Identify the parasite.
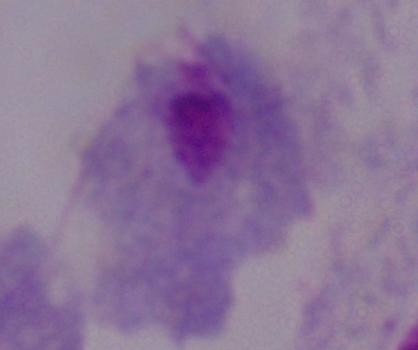
This is a trichomonad.

Summary:
  - Modality: photomicrograph
  - Magnification: 1000x